Name the parasite shown.
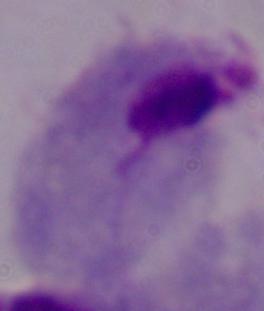
A trichomonad.

Summary:
  - Magnification: 1000x
  - Modality: photomicrograph